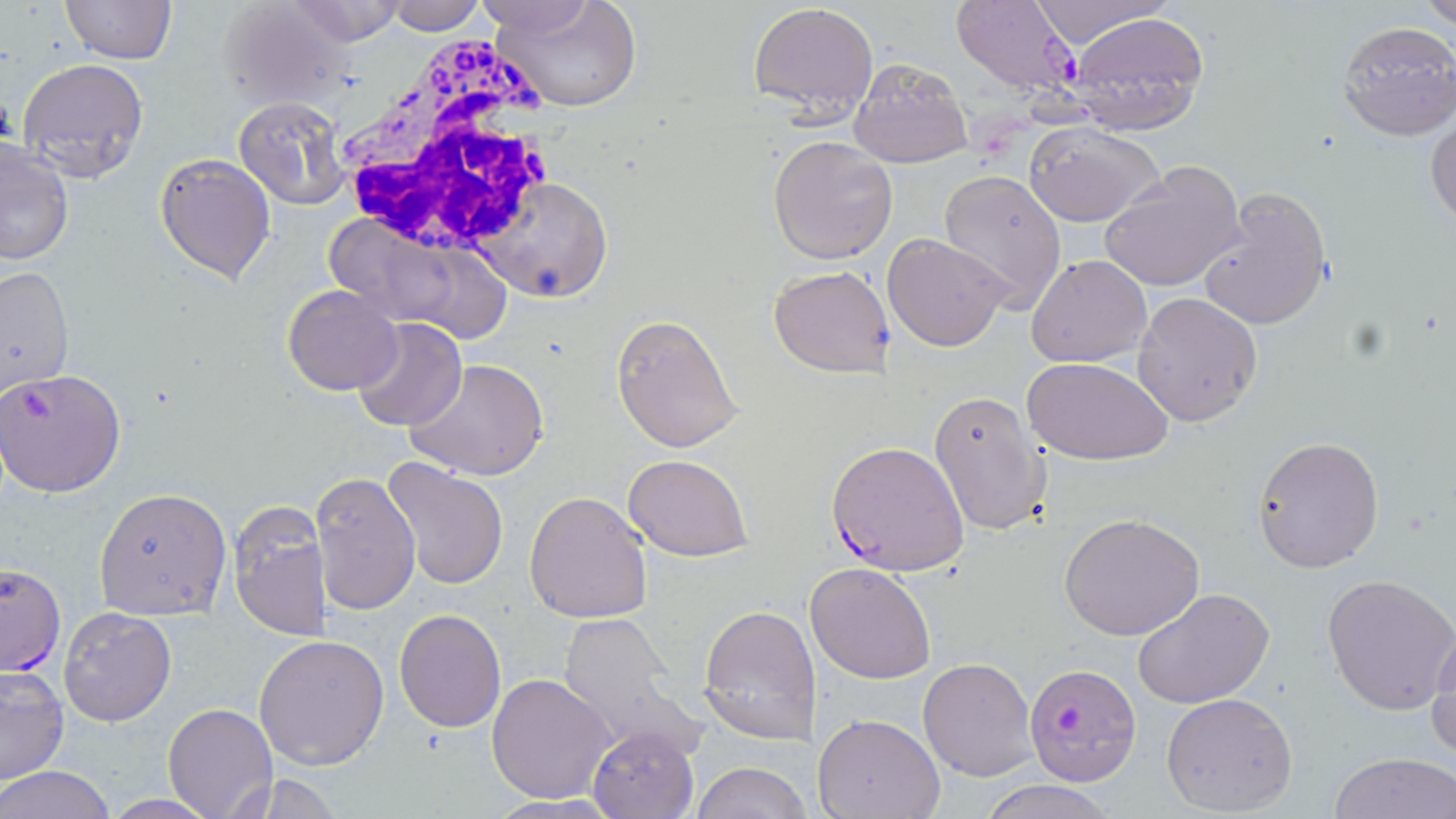

{
  "slide_level_diagnosis": "Plasmodium falciparum",
  "white_blood_cell_locations": "approximate bounding boxes as named x1/y1/x2/y2 corners in pixels: (x1=332, y1=34, x2=567, y2=263)",
  "stain": "May-Grünwald-Giemsa",
  "plasmodium_falciparum_infected_red_blood_cell_locations": "approximate bounding boxes as named x1/y1/x2/y2 corners in pixels: (x1=951, y1=0, x2=1080, y2=98), (x1=0, y1=368, x2=127, y2=498), (x1=825, y1=439, x2=971, y2=575), (x1=0, y1=562, x2=66, y2=677), (x1=1023, y1=663, x2=1142, y2=785)",
  "magnification": "1000x",
  "modality": "light microscopy",
  "preparation": "thin blood smear",
  "field_of_view": "single",
  "platelet_locations": "approximate bounding boxes as named x1/y1/x2/y2 corners in pixels: (x1=971, y1=103, x2=1039, y2=170)",
  "uninfected_red_blood_cell_locations": "approximate bounding boxes as named x1/y1/x2/y2 corners in pixels: (x1=282, y1=0, x2=411, y2=45), (x1=488, y1=0, x2=643, y2=112), (x1=1023, y1=0, x2=1177, y2=48), (x1=1422, y1=0, x2=1456, y2=31), (x1=59, y1=1, x2=177, y2=66), (x1=386, y1=1, x2=486, y2=35), (x1=469, y1=1, x2=598, y2=35), (x1=748, y1=1, x2=878, y2=124), (x1=213, y1=2, x2=353, y2=109), (x1=1068, y1=12, x2=1207, y2=133), (x1=1335, y1=21, x2=1456, y2=140), (x1=17, y1=57, x2=149, y2=185), (x1=849, y1=57, x2=972, y2=168), (x1=232, y1=96, x2=351, y2=208), (x1=1426, y1=108, x2=1456, y2=231), (x1=1024, y1=121, x2=1165, y2=226), (x1=767, y1=135, x2=898, y2=264), (x1=0, y1=141, x2=74, y2=266), (x1=154, y1=151, x2=276, y2=285), (x1=1099, y1=159, x2=1248, y2=293), (x1=938, y1=168, x2=1067, y2=313), (x1=472, y1=176, x2=612, y2=302), (x1=1194, y1=184, x2=1334, y2=332), (x1=328, y1=221, x2=506, y2=340), (x1=883, y1=233, x2=1010, y2=352), (x1=1026, y1=255, x2=1152, y2=368), (x1=769, y1=265, x2=896, y2=378), (x1=1, y1=267, x2=74, y2=396), (x1=282, y1=284, x2=402, y2=396), (x1=1131, y1=292, x2=1262, y2=428), (x1=611, y1=313, x2=745, y2=453), (x1=351, y1=318, x2=468, y2=434), (x1=1023, y1=356, x2=1175, y2=466), (x1=407, y1=358, x2=550, y2=481), (x1=928, y1=389, x2=1052, y2=536), (x1=1252, y1=436, x2=1384, y2=573), (x1=623, y1=454, x2=752, y2=561), (x1=381, y1=458, x2=510, y2=592), (x1=311, y1=470, x2=421, y2=618), (x1=93, y1=488, x2=232, y2=620), (x1=523, y1=491, x2=654, y2=625), (x1=229, y1=506, x2=330, y2=643), (x1=1059, y1=513, x2=1204, y2=640), (x1=805, y1=562, x2=936, y2=684), (x1=1324, y1=572, x2=1456, y2=714), (x1=1133, y1=587, x2=1275, y2=708), (x1=699, y1=603, x2=820, y2=744), (x1=59, y1=607, x2=176, y2=728), (x1=394, y1=608, x2=506, y2=731), (x1=557, y1=613, x2=689, y2=745), (x1=1425, y1=624, x2=1456, y2=763), (x1=254, y1=634, x2=389, y2=771), (x1=918, y1=656, x2=1038, y2=780), (x1=0, y1=667, x2=69, y2=786), (x1=486, y1=673, x2=617, y2=804), (x1=1159, y1=691, x2=1298, y2=815), (x1=164, y1=702, x2=277, y2=818), (x1=814, y1=713, x2=946, y2=819), (x1=588, y1=722, x2=700, y2=819), (x1=1331, y1=753, x2=1456, y2=819), (x1=691, y1=762, x2=808, y2=819), (x1=1, y1=766, x2=114, y2=819), (x1=220, y1=773, x2=346, y2=817), (x1=977, y1=777, x2=1115, y2=819), (x1=484, y1=793, x2=624, y2=818), (x1=98, y1=795, x2=223, y2=818)",
  "image_size": "1456×819 pixels"
}